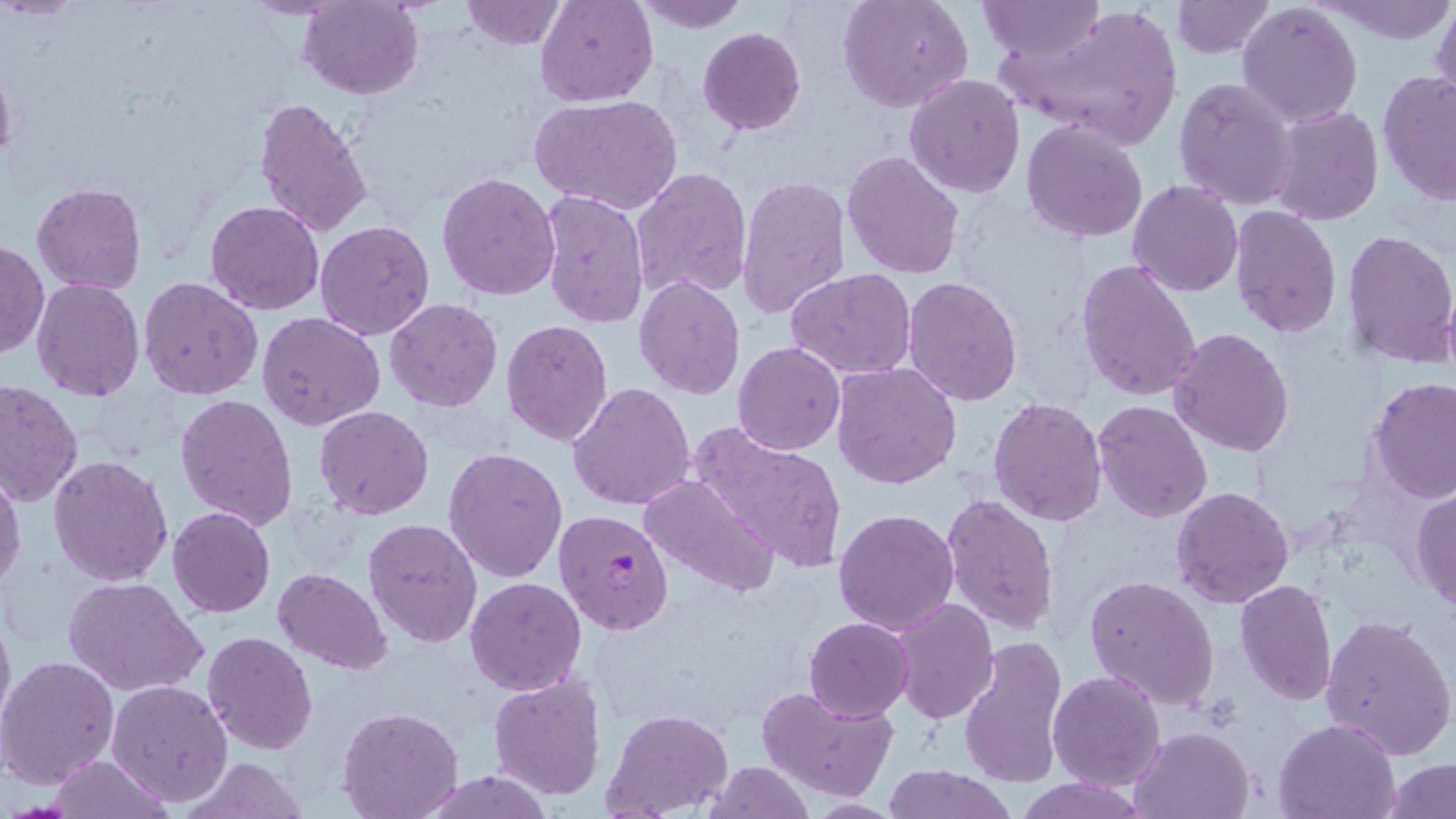

Approximate bounding boxes as (x1,y1)-(x2,y2) corner pairs in pixels. Uninfected red blood cell locations: (460,0)-(567,48), (536,0)-(657,106), (636,0)-(749,32), (838,0)-(973,112), (1169,0)-(1276,57), (1324,0)-(1453,44), (298,1)-(422,100), (979,1)-(1104,62), (1432,1)-(1455,112), (1237,3)-(1364,128), (1002,4)-(1186,149), (698,28)-(806,135), (0,53)-(17,173), (1378,69)-(1456,205), (904,74)-(1025,199), (1173,77)-(1297,211), (532,93)-(683,215), (253,97)-(375,235), (1269,104)-(1383,225), (1021,120)-(1148,243), (842,151)-(965,279), (630,167)-(751,302), (437,172)-(559,300), (737,176)-(851,321), (1127,180)-(1244,297), (31,182)-(147,295), (539,190)-(649,330), (204,199)-(325,314), (1228,204)-(1343,338), (314,220)-(435,339), (1341,228)-(1456,367), (1,239)-(47,358), (1076,258)-(1201,402), (787,268)-(915,380), (634,275)-(745,400), (139,276)-(263,399), (902,276)-(1024,407), (31,277)-(145,401), (385,298)-(503,413), (258,311)-(385,430), (502,319)-(612,445), (1167,328)-(1295,460), (732,341)-(845,455), (832,361)-(961,489), (1368,377)-(1456,503), (1,379)-(82,505), (567,383)-(695,511), (175,394)-(298,530), (988,395)-(1108,526), (1093,400)-(1213,522), (314,404)-(433,519), (686,421)-(850,573), (442,447)-(568,583), (48,455)-(173,585), (0,467)-(26,597), (640,474)-(781,599), (1170,485)-(1294,610), (1410,486)-(1456,611), (940,494)-(1059,637), (168,506)-(276,617), (833,508)-(959,635), (363,518)-(484,650), (272,568)-(392,674), (1084,574)-(1220,710), (63,576)-(207,696), (465,577)-(585,694), (1234,579)-(1337,706), (888,595)-(998,724), (0,602)-(15,742), (1320,613)-(1455,760), (804,617)-(914,721), (202,630)-(318,753), (958,636)-(1070,788), (0,657)-(120,789), (1048,670)-(1166,791), (487,673)-(607,802), (106,680)-(234,806), (757,684)-(899,802), (336,706)-(463,819), (601,707)-(731,816), (1273,716)-(1402,819), (1130,724)-(1255,818), (48,755)-(172,818), (179,757)-(311,819), (705,761)-(815,818), (1383,761)-(1456,818), (881,765)-(1016,819), (423,771)-(553,818), (1014,778)-(1148,818), (799,799)-(907,817). Plasmodium falciparum-infected red blood cell locations: (553,508)-(674,635). Slide-level diagnosis: Plasmodium falciparum. Image is 1456×819 pixels. Optical microscopy. 1000x magnification. May-Grünwald-Giemsa-stained preparation. Thin blood smear. One field of a larger specimen.